Classify this cell by malaria status.
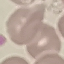

It is uninfected.

{
  "capture": "smartphone through the microscope eyepiece",
  "image_type": "cell patch, automatically extracted from a larger field of view and resized to 64 × 64 pixels",
  "stain": "Giemsa",
  "preparation": "thin blood film"
}